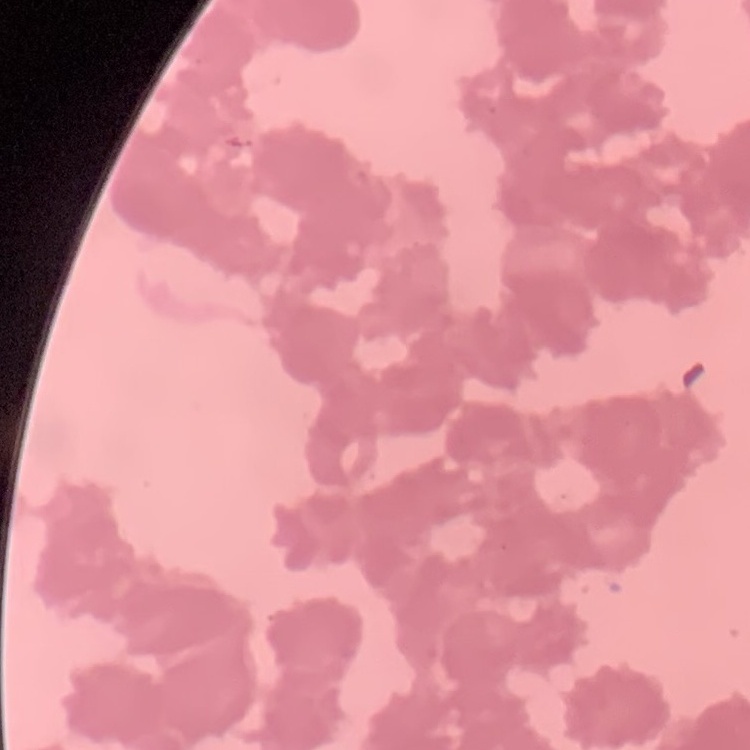

Summary:
  - Red blood cell morphology: rouleaux formation
  - Image type: one tile cut from a larger photomicrograph
  - Stain: Field's or Giemsa
  - Preparation: thin peripheral smear